Locate every Plasmodium ovale-infected red blood cell.
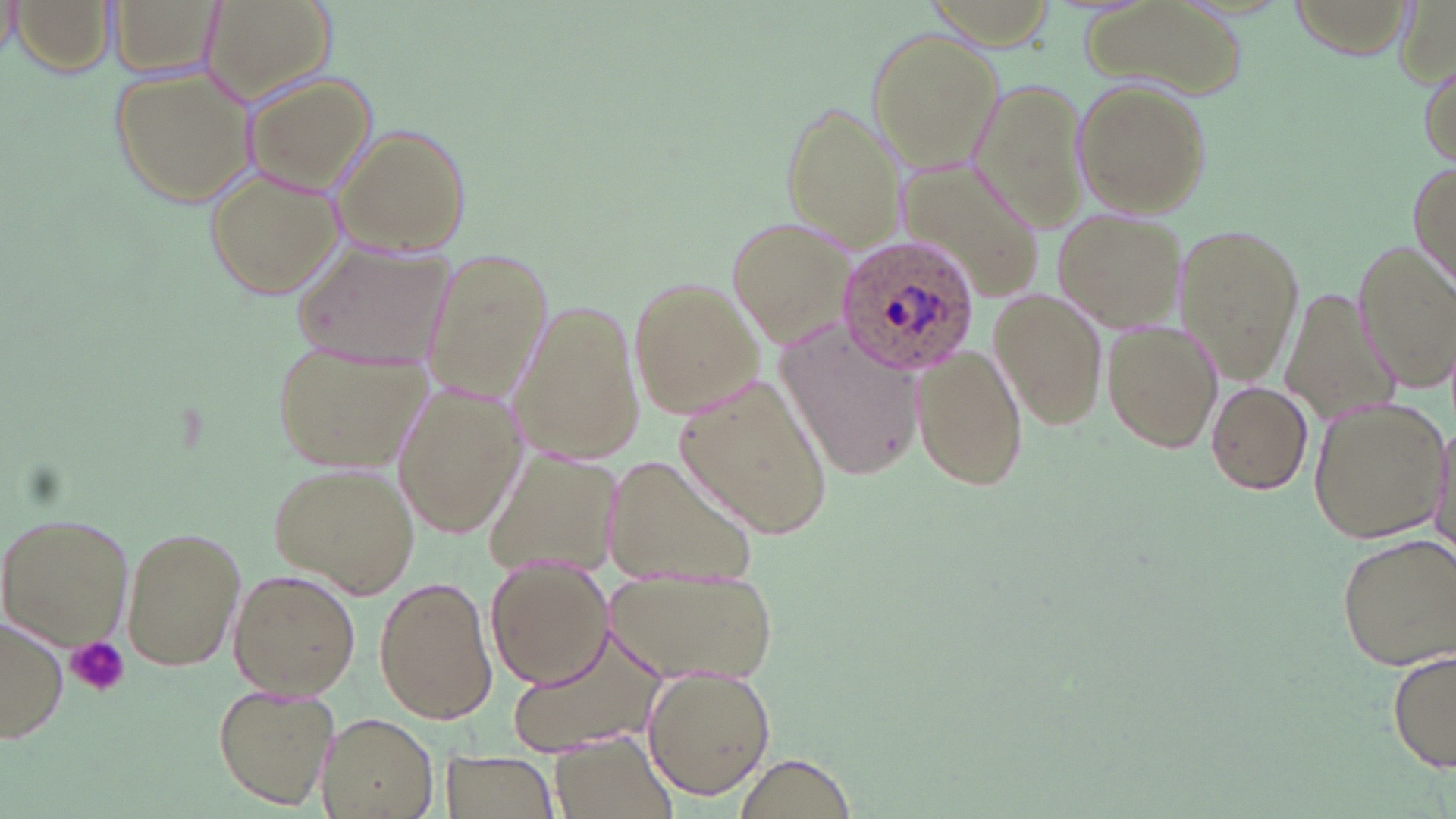

Approximate bounding boxes as (x1, y1, x2, y2) in pixels.
Plasmodium ovale-infected red blood cells: (836, 232, 979, 378).

Summary:
  - Platelet locations: (66, 636, 130, 697)
  - Uninfected red blood cell locations: (11, 0, 116, 75), (110, 0, 222, 77), (200, 0, 338, 107), (1, 1, 23, 58), (1081, 1, 1248, 102), (864, 27, 1002, 172), (1417, 54, 1454, 170), (108, 63, 262, 208), (240, 73, 376, 193), (972, 78, 1099, 238), (1074, 81, 1209, 217), (780, 100, 904, 250), (331, 124, 474, 255), (887, 159, 1046, 297), (1408, 162, 1455, 286), (203, 168, 341, 299), (1053, 210, 1185, 332), (728, 218, 859, 352), (1176, 223, 1305, 383), (1353, 238, 1454, 394), (299, 245, 455, 370), (419, 248, 553, 403), (630, 274, 769, 420), (1281, 285, 1394, 429), (989, 289, 1104, 433), (508, 300, 648, 462), (1102, 319, 1223, 455), (776, 322, 926, 482), (265, 336, 429, 475), (911, 342, 1029, 494), (676, 373, 834, 541), (392, 380, 526, 538), (1204, 381, 1314, 496), (1307, 398, 1449, 544), (1432, 417, 1456, 560), (485, 446, 625, 576), (596, 453, 764, 596), (269, 463, 418, 596), (1, 512, 134, 651), (120, 524, 246, 672), (1335, 535, 1454, 671), (486, 559, 613, 689), (606, 567, 778, 687), (229, 570, 361, 698), (374, 577, 498, 725), (1, 614, 67, 744), (506, 625, 669, 755), (1391, 648, 1456, 776), (639, 662, 776, 800), (212, 684, 339, 810), (315, 710, 438, 818), (549, 731, 677, 819), (437, 750, 560, 819), (736, 753, 857, 818)
  - Slide-level diagnosis: Plasmodium ovale
  - Field of view: single
  - Magnification: 1000x
  - Preparation: thin blood smear
  - Image size: 1456×819 pixels
  - Stain: May-Grünwald-Giemsa
  - Modality: optical microscopy